Report the malaria status of this cell.
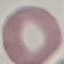

Uninfected.

stain = Giemsa
preparation = thin blood film
capture = smartphone through the microscope eyepiece
image type = cell patch, automatically extracted from a larger field of view and resized to 64 × 64 pixels